Assess this cell for malaria.
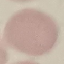
Uninfected.

capture = smartphone camera at the microscope eyepiece
preparation = thin blood smear
stain = Giemsa
image type = cell patch, automatically extracted from a larger field of view and resized to 64 × 64 pixels